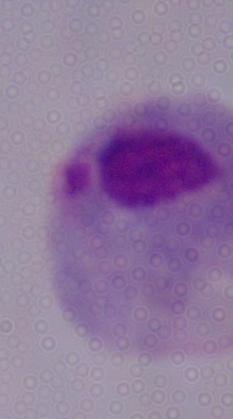 Photomicrograph. A trichomonad is shown. 1000x magnification.